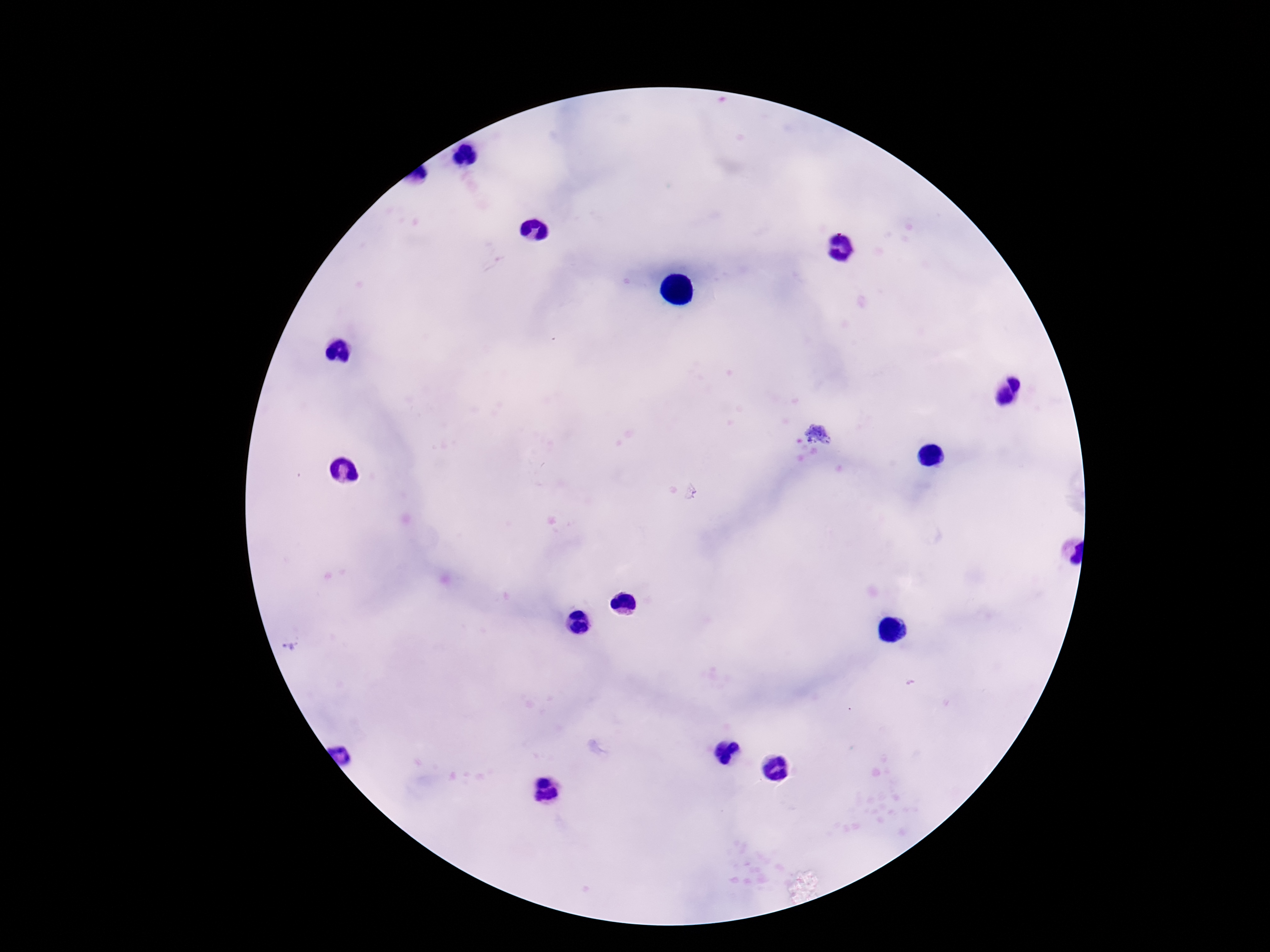

Approximate centers as (x, y) in pixels.
Summary:
  - Plasmodium parasite locations: (818, 434), (288, 647)
  - Magnification: 100x
  - Patient malaria status: infected
  - Capture: smartphone camera through the microscope eyepiece
  - Field of view: single
  - Stain: Giemsa
  - Image size: 1270×952 pixels
  - Preparation: thick blood smear